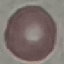
Malaria status: uninfected. Giemsa stain. Thin blood film. Photographed with a smartphone camera at the microscope eyepiece. Cell patch, automatically extracted from a larger field of view and resized to 64 × 64 pixels.